Assess this cell for malaria.
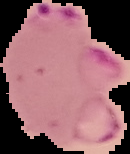
Parasitized.

image type = segmented cell region with the area outside set to black
image size = 130×154 pixels
preparation = thin blood film